Name the blood parasite species.
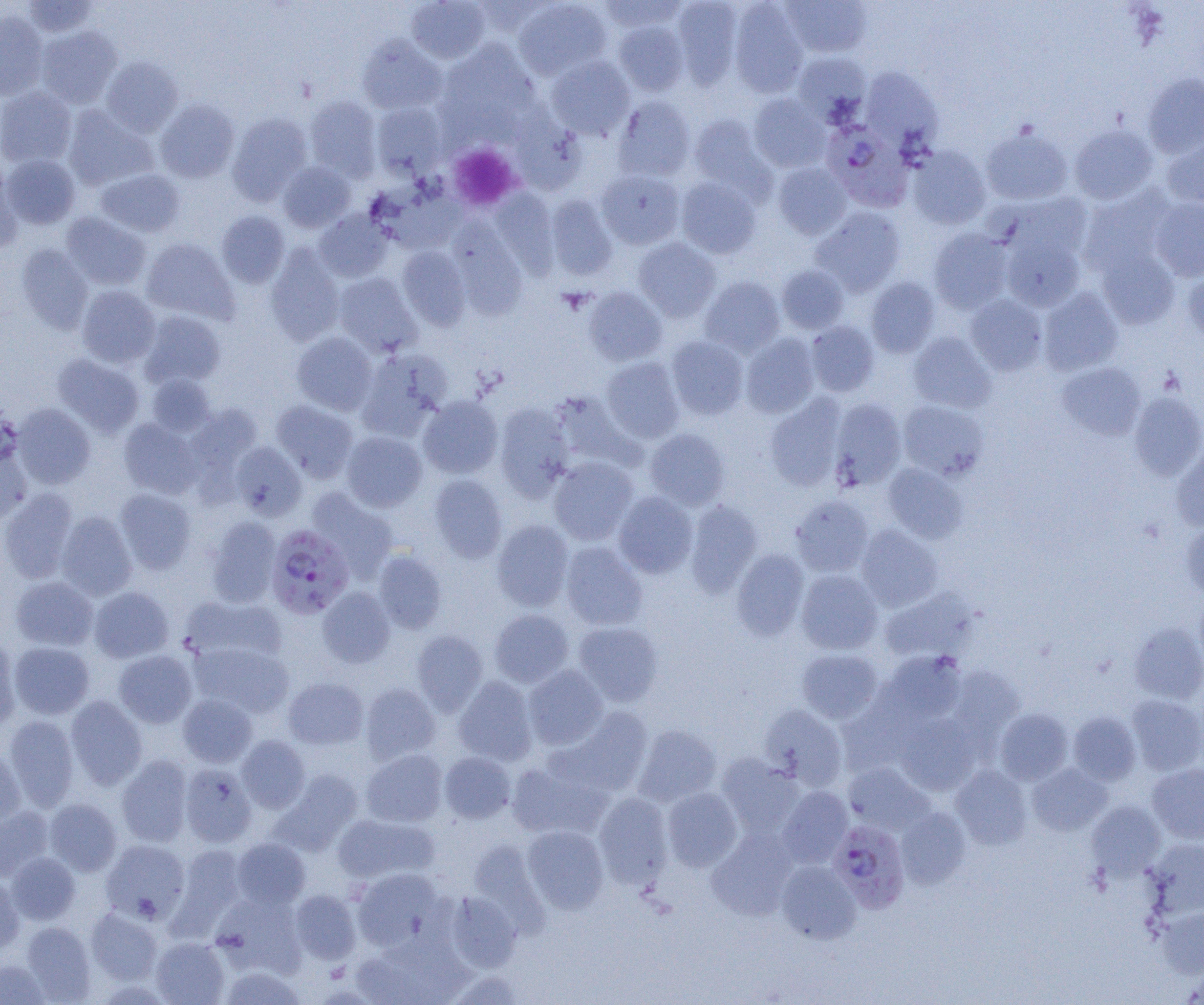
Plasmodium falciparum.

uninfected_red_blood_cell_locations: 'approximate bounding boxes as [x1, y1, x2, y2] in pixels: [405, 0, 490, 63], [513, 0, 612, 80], [599, 0, 686, 32], [672, 0, 742, 89], [781, 0, 872, 58], [21, 1, 100, 38], [729, 1, 809, 97], [0, 11, 48, 100], [614, 21, 689, 95], [35, 26, 122, 108], [357, 35, 447, 115], [437, 41, 540, 135], [792, 52, 871, 123], [546, 56, 635, 140], [101, 57, 183, 136], [861, 68, 942, 150], [1143, 74, 1204, 158], [0, 86, 77, 169], [749, 94, 831, 172], [305, 96, 382, 181], [613, 96, 695, 181], [155, 99, 239, 183], [371, 103, 447, 178], [63, 106, 157, 190], [510, 112, 588, 195], [227, 113, 312, 205], [689, 114, 770, 193], [981, 125, 1072, 206], [1070, 125, 1157, 205], [1162, 134, 1204, 208], [906, 147, 991, 229], [2, 154, 80, 229], [0, 162, 21, 254], [278, 162, 356, 232], [772, 162, 852, 239], [95, 168, 185, 237], [596, 169, 684, 249], [676, 177, 761, 259], [375, 181, 467, 254], [1079, 188, 1174, 277], [491, 189, 559, 277], [1004, 193, 1093, 264], [546, 195, 618, 280], [1150, 197, 1204, 281], [811, 207, 905, 296], [314, 210, 393, 282], [216, 211, 290, 287], [62, 212, 151, 290], [449, 219, 528, 318], [929, 228, 1013, 313], [1001, 234, 1085, 312], [141, 238, 238, 324], [633, 238, 721, 322], [16, 243, 93, 333], [265, 245, 344, 346], [397, 246, 471, 330], [1096, 248, 1180, 329], [777, 265, 848, 334], [1183, 267, 1204, 344], [333, 273, 422, 357], [700, 276, 785, 357], [866, 277, 940, 358], [77, 285, 160, 368], [583, 287, 667, 366], [1039, 288, 1123, 375], [965, 294, 1047, 376], [140, 311, 226, 388], [806, 321, 879, 396], [908, 331, 996, 413], [291, 332, 378, 415], [740, 333, 820, 418], [666, 336, 748, 419], [357, 348, 451, 439], [53, 354, 144, 437], [600, 357, 684, 443], [1057, 362, 1146, 440], [146, 374, 215, 436], [549, 391, 637, 469], [1129, 391, 1204, 480], [765, 394, 846, 490], [418, 395, 502, 478], [829, 398, 906, 490], [272, 400, 358, 482], [898, 400, 988, 481], [12, 403, 95, 489], [185, 403, 262, 481], [495, 403, 574, 500], [119, 418, 202, 499], [645, 428, 729, 510], [341, 430, 427, 512], [230, 442, 307, 520], [0, 443, 32, 524], [1171, 446, 1204, 530], [549, 456, 638, 545], [883, 463, 967, 543], [429, 474, 507, 563], [0, 488, 78, 583], [307, 488, 399, 581], [114, 489, 196, 574], [613, 492, 698, 578], [790, 495, 873, 576], [685, 501, 762, 597], [57, 511, 137, 600], [206, 516, 282, 607], [492, 519, 573, 611], [1181, 523, 1204, 598], [856, 525, 943, 612], [493, 530, 647, 618], [561, 542, 647, 630], [732, 549, 809, 640], [372, 550, 447, 633], [796, 570, 883, 654], [10, 576, 98, 650], [89, 586, 173, 663], [318, 587, 395, 667], [879, 588, 977, 663], [1195, 593, 1204, 672], [181, 595, 285, 666], [490, 609, 573, 688], [574, 622, 664, 706], [1130, 622, 1204, 702], [411, 630, 487, 715], [0, 640, 20, 730], [9, 641, 94, 719], [192, 642, 294, 718], [797, 649, 883, 723], [114, 650, 197, 727], [878, 650, 966, 725], [523, 664, 608, 750], [947, 666, 1024, 748], [454, 676, 538, 766], [283, 677, 368, 749], [361, 682, 441, 764], [178, 694, 257, 767], [1127, 694, 1204, 775], [65, 696, 147, 789], [759, 704, 847, 789], [555, 707, 653, 797], [994, 708, 1073, 785], [1069, 712, 1141, 786], [896, 714, 981, 795], [3, 715, 79, 810], [634, 725, 721, 806], [237, 736, 310, 813], [0, 749, 25, 824], [361, 749, 447, 827], [439, 752, 516, 823], [716, 753, 803, 837], [117, 755, 193, 847], [507, 757, 612, 840], [180, 763, 256, 847], [844, 763, 933, 835], [1027, 763, 1112, 835], [1147, 763, 1204, 843], [950, 765, 1031, 849], [272, 770, 363, 855], [777, 786, 852, 867], [662, 788, 742, 871], [593, 793, 672, 888], [45, 799, 121, 876], [1087, 801, 1166, 879], [0, 806, 53, 882], [896, 807, 971, 889], [334, 813, 439, 884], [523, 825, 609, 913], [706, 828, 799, 920], [232, 838, 310, 909], [101, 839, 190, 924], [1145, 839, 1204, 918], [170, 844, 247, 936], [6, 852, 80, 925], [776, 860, 861, 943], [351, 868, 446, 951], [0, 876, 25, 956], [289, 890, 361, 964], [445, 891, 522, 972], [212, 893, 307, 976], [86, 907, 162, 985], [1158, 907, 1204, 978], [21, 922, 96, 1002], [151, 937, 229, 1005], [351, 944, 459, 1005], [0, 959, 51, 1005], [1181, 964, 1204, 1005], [220, 967, 305, 1005], [449, 971, 526, 1005]'
modality: light microscopy
preparation: thin blood film
plasmodium_falciparum_infected_red_blood_cell_locations: 'approximate bounding boxes as [x1, y1, x2, y2] in pixels: [823, 121, 912, 210], [265, 525, 354, 619], [828, 820, 911, 912]'
field_of_view: one of a larger specimen
image_size: 1204×1005 pixels
platelet_locations: 'approximate bounding boxes as [x1, y1, x2, y2] in pixels: [448, 143, 522, 211]'
magnification: 1000x